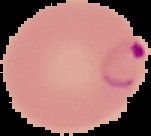

malaria status = parasitized
preparation = thin blood smear
image type = cell region segmented out of the field of view; surrounding area masked to black
image size = 151×136 pixels